Comment on the morphology of the erythrocytes.
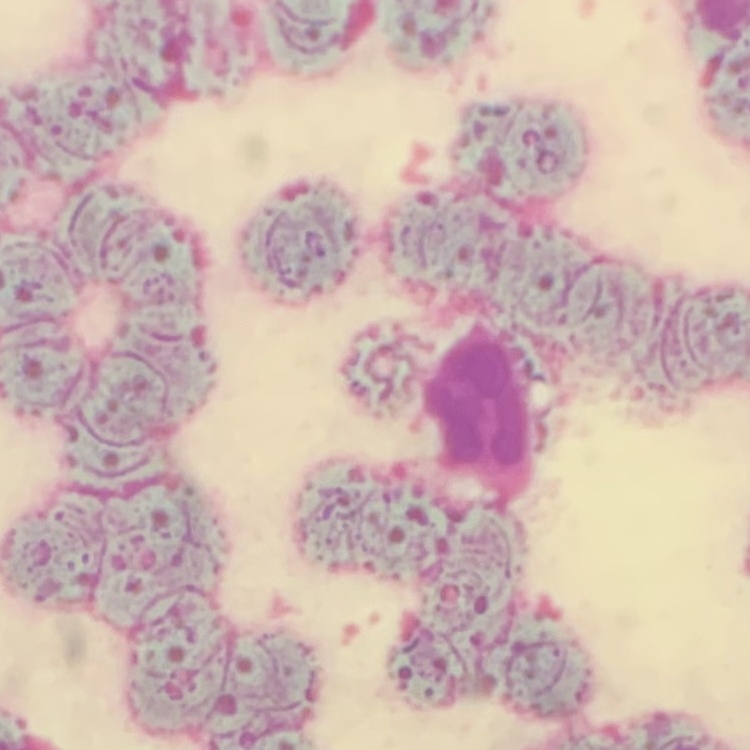
They show rouleaux formation.

image type = one tile cut from a larger photomicrograph
preparation = thin blood film
stain = Field's or Giemsa